Outline each Plasmodium vivax-infected red blood cell.
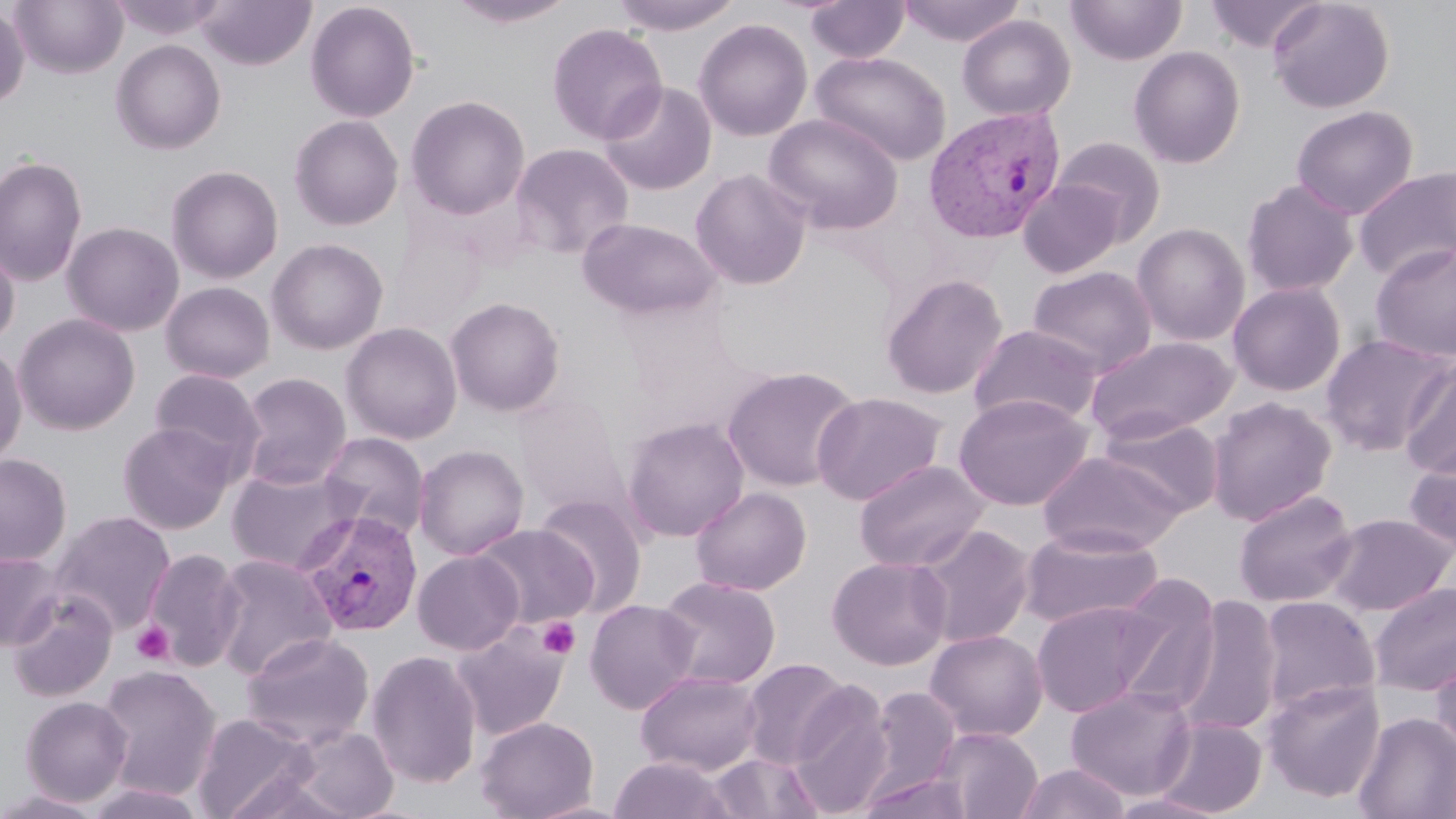

Approximate bounding boxes as (x1,y1)-(x2,y2) corner pairs in pixels.
Plasmodium vivax-infected red blood cells: (923,105)-(1067,244), (296,510)-(424,636).

Platelet locations: (538,617)-(580,659), (131,621)-(175,665). Uninfected red blood cell locations: (9,0)-(127,79), (196,0)-(316,70), (443,0)-(580,28), (609,0)-(745,35), (806,0)-(909,63), (896,0)-(1027,46), (1065,0)-(1187,66), (1204,0)-(1321,53), (1268,0)-(1394,114), (305,1)-(420,123), (0,5)-(30,108), (957,14)-(1076,121), (693,19)-(813,142), (546,23)-(668,145), (111,39)-(226,154), (1128,46)-(1246,169), (810,50)-(951,166), (598,81)-(717,196), (406,95)-(530,220), (1290,105)-(1418,220), (764,113)-(904,234), (289,115)-(404,231), (1051,137)-(1168,244), (509,142)-(635,260), (0,156)-(87,288), (166,165)-(284,284), (1353,166)-(1456,283), (689,168)-(812,290), (1017,179)-(1125,278), (1241,179)-(1359,297), (578,218)-(722,320), (62,221)-(184,336), (1132,222)-(1250,346), (266,238)-(389,355), (0,240)-(20,348), (1369,242)-(1456,364), (1027,265)-(1157,376), (881,274)-(1008,399), (160,281)-(276,383), (1227,282)-(1346,396), (444,297)-(566,416), (13,313)-(140,436), (340,322)-(463,444), (969,323)-(1103,428), (1320,332)-(1454,456), (1084,334)-(1238,443), (0,343)-(27,468), (1399,357)-(1456,480), (722,365)-(862,491), (148,367)-(266,475), (237,372)-(352,489), (811,391)-(947,505), (953,392)-(1094,510), (1206,396)-(1338,525), (514,397)-(629,518), (1095,413)-(1225,517), (622,417)-(750,542), (117,422)-(235,535), (318,431)-(430,541), (1403,443)-(1456,557), (413,444)-(529,560), (1037,450)-(1188,556), (0,453)-(72,567), (854,459)-(989,573), (227,464)-(363,574), (690,486)-(811,596), (1233,490)-(1358,608), (534,495)-(648,616), (49,510)-(176,634), (1323,513)-(1455,616), (473,524)-(599,628), (911,524)-(1035,650), (1017,526)-(1165,630), (143,548)-(246,670), (412,550)-(524,655), (0,553)-(64,651), (210,553)-(336,681), (827,555)-(953,670), (655,575)-(782,690), (1108,576)-(1223,714), (1368,581)-(1456,696), (6,590)-(118,702), (1174,595)-(1283,737), (1257,596)-(1381,717), (584,599)-(701,715), (1031,600)-(1167,718), (451,621)-(571,741), (925,629)-(1048,742), (240,631)-(375,750), (366,649)-(483,789), (1430,649)-(1456,763), (740,657)-(853,770), (95,664)-(222,800), (635,670)-(765,776), (1262,679)-(1386,802), (789,682)-(895,819), (1064,685)-(1197,800), (869,687)-(961,794), (19,696)-(133,806), (1353,711)-(1456,819), (191,713)-(316,819), (475,715)-(599,819), (1151,716)-(1268,817), (284,725)-(399,819), (934,727)-(1042,819), (704,751)-(826,819), (608,756)-(734,819), (1016,762)-(1131,819), (857,772)-(976,819), (81,782)-(211,819), (0,787)-(106,818), (1106,792)-(1229,819). Slide-level diagnosis: Plasmodium vivax. Single field of view. Image is 1456×819 pixels. Thin blood film. Captured at 1000x magnification. Light microscopy. May-Grünwald-Giemsa stain.